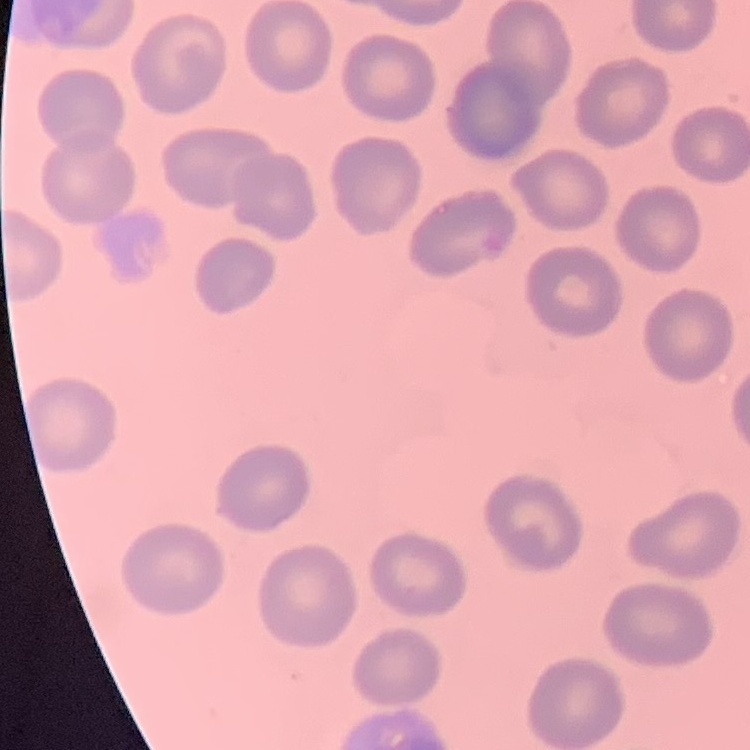 The red blood cells exhibit no rouleaux formation. One tile cut from a larger photomicrograph. Field's or Giemsa stain. Thin peripheral smear.